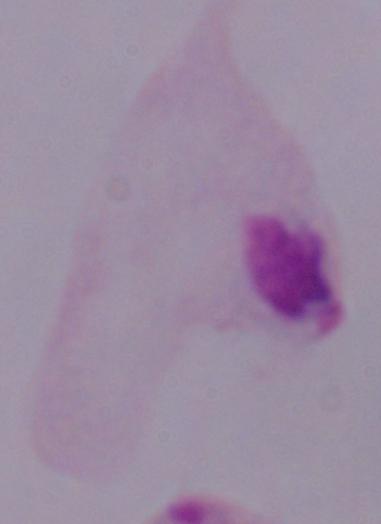

Summary:
  - Modality: micrograph
  - Magnification: 1000x
  - Identification: trichomonad